Classify this cell by malaria status.
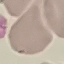
Uninfected.

Summary:
  - Capture: smartphone camera at the microscope eyepiece
  - Image type: automatically extracted cell patch, resized to 64 × 64 pixels
  - Stain: Giemsa
  - Preparation: thin smear